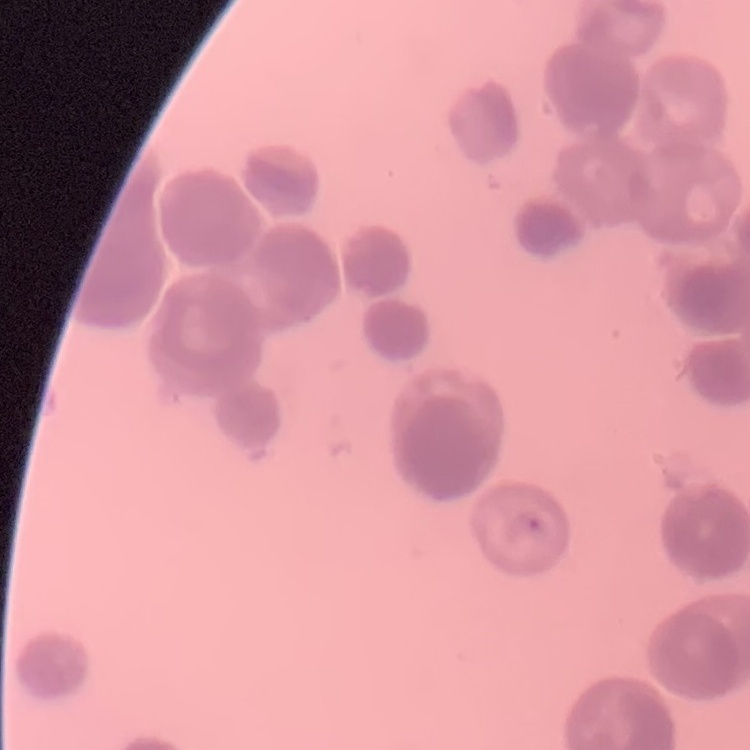

Summary:
  - Erythrocyte morphology: rouleaux formation
  - Image type: one tile cut from a larger photomicrograph
  - Stain: Field's or Giemsa
  - Preparation: thin blood smear